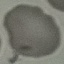

result = no malaria parasites detected
image type = cell patch, automatically extracted from a larger field of view and resized to 64 × 64 pixels
stain = Giemsa
preparation = thin blood smear
capture = smartphone through the microscope eyepiece